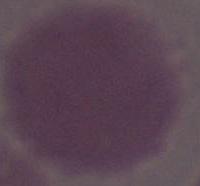
Photomicrograph. A red blood cell is seen. Captured at 1000x magnification.